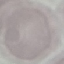

Result: no malaria parasites seen. Automatically extracted cell patch, resized to 64 × 64 pixels. Photographed with a smartphone camera at the microscope eyepiece. Thin blood smear. Giemsa stain.